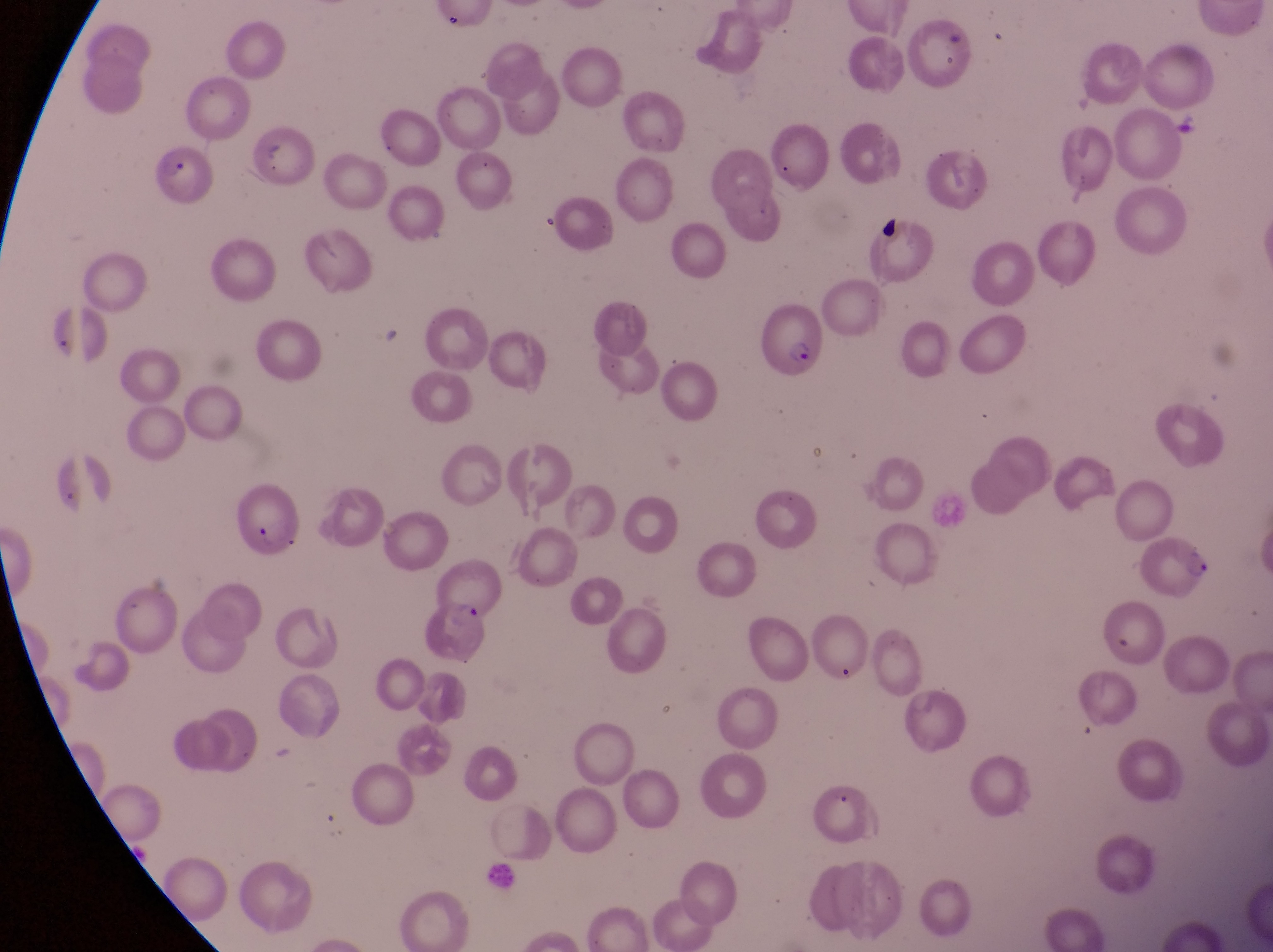
Approximate bounding boxes as {left, top, right, bottom} in pixels.
Summary:
  - Parasitised red blood cell locations: {152, 142, 210, 210}, {757, 312, 832, 389}, {239, 482, 309, 564}, {1141, 532, 1215, 600}, {417, 597, 492, 665}
  - Country: Uganda
  - Image size: 1273×952 pixels
  - Capture: smartphone photograph through the eyepiece of an Olympus CX-23 microscope
  - Field of view: single
  - Magnification: 1000x
  - Preparation: thin blood film